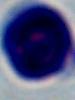
modality = photomicrograph
identification = white blood cell
magnification = 1000x